Assess for malaria.
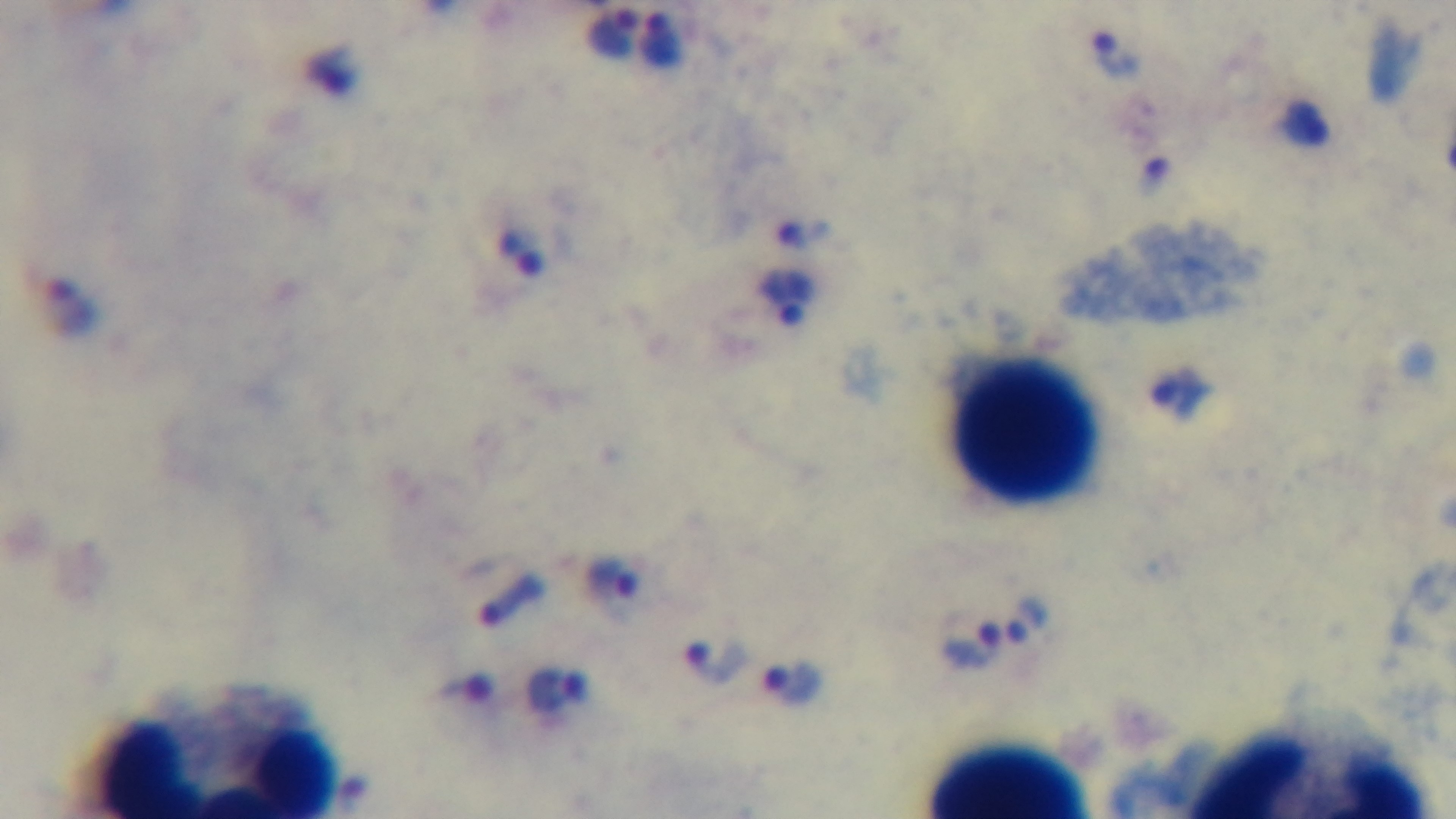

Infected.

field of view = single
stain = Giemsa
capture = mounted 4K digital camera
objective = 100x oil immersion
modality = light microscopy
preparation = thick